Identify the parasite.
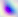

Toxoplasma gondii.

{
  "magnification": "400x",
  "modality": "photomicrograph"
}